State which parasite is depicted.
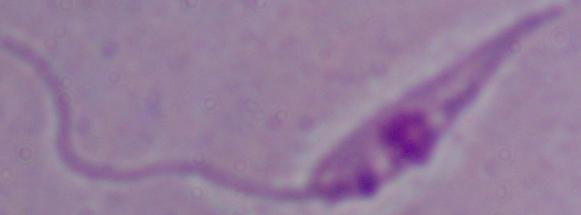

Leishmania.

magnification = 1000x
modality = photomicrograph